Give the extent of all Plasmodium falciparum-infected red blood cells.
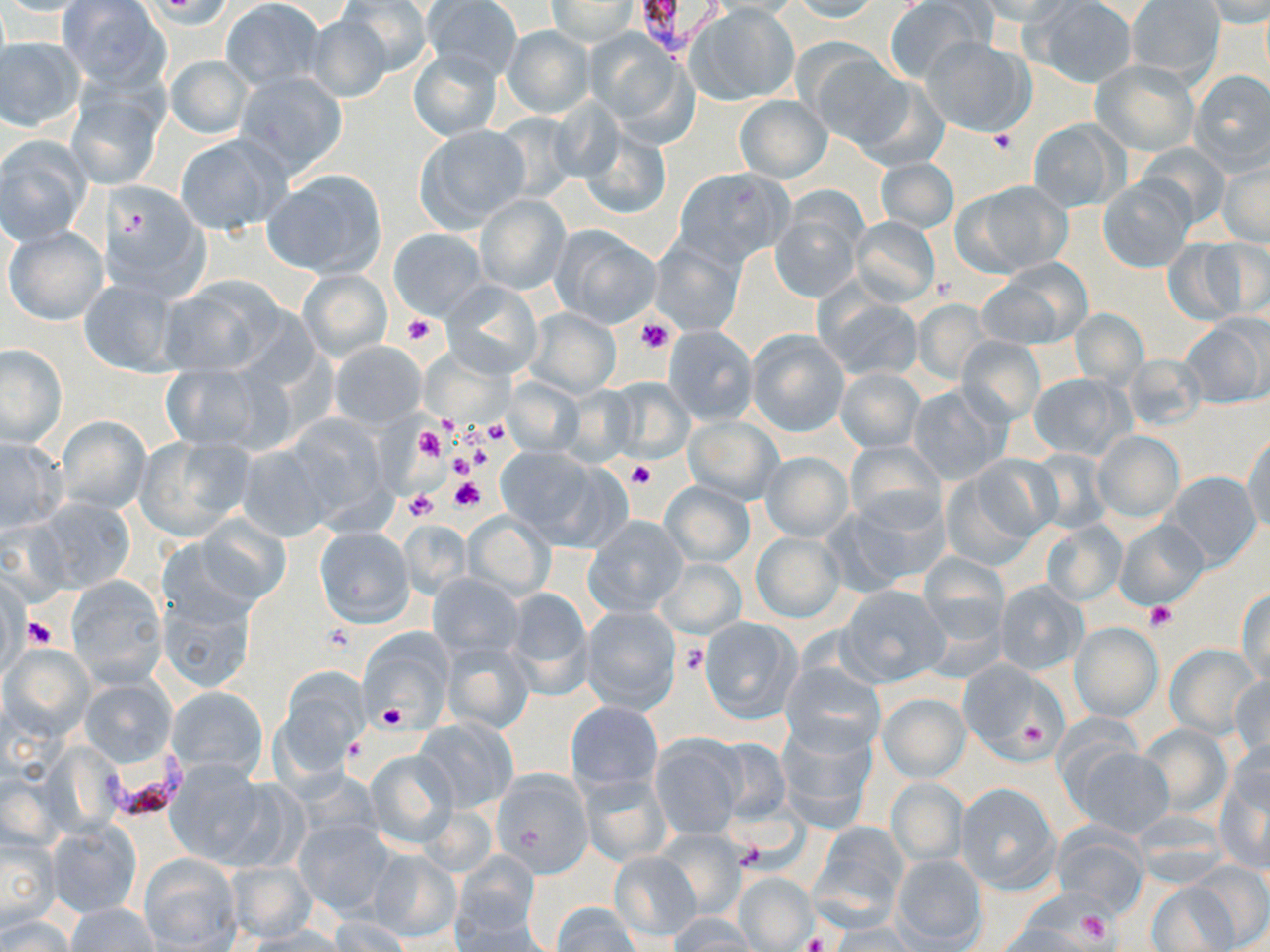
Approximate bounding boxes as named x1/y1/x2/y2 corners in pixels.
Plasmodium falciparum-infected red blood cells: (x1=635, y1=0, x2=724, y2=55), (x1=94, y1=754, x2=197, y2=818).

Summary:
  - Platelet locations: (x1=985, y1=128, x2=1019, y2=156), (x1=402, y1=313, x2=435, y2=346), (x1=637, y1=318, x2=674, y2=355), (x1=483, y1=419, x2=513, y2=445), (x1=414, y1=424, x2=447, y2=463), (x1=446, y1=450, x2=477, y2=478), (x1=627, y1=459, x2=655, y2=488), (x1=448, y1=476, x2=483, y2=512), (x1=406, y1=489, x2=438, y2=520), (x1=1145, y1=601, x2=1177, y2=631), (x1=26, y1=616, x2=55, y2=647), (x1=322, y1=624, x2=354, y2=652), (x1=678, y1=642, x2=709, y2=675), (x1=379, y1=705, x2=406, y2=731), (x1=1015, y1=719, x2=1049, y2=753), (x1=1075, y1=910, x2=1110, y2=944), (x1=803, y1=932, x2=827, y2=952)
  - Uninfected red blood cell locations: (x1=336, y1=0, x2=434, y2=78), (x1=419, y1=0, x2=522, y2=81), (x1=703, y1=0, x2=810, y2=16), (x1=790, y1=0, x2=883, y2=22), (x1=979, y1=0, x2=1076, y2=24), (x1=1125, y1=0, x2=1225, y2=81), (x1=0, y1=1, x2=99, y2=17), (x1=57, y1=1, x2=167, y2=87), (x1=221, y1=1, x2=325, y2=89), (x1=547, y1=1, x2=638, y2=45), (x1=884, y1=1, x2=991, y2=83), (x1=1027, y1=1, x2=1137, y2=88), (x1=1204, y1=1, x2=1270, y2=27), (x1=686, y1=4, x2=799, y2=106), (x1=304, y1=14, x2=393, y2=104), (x1=500, y1=26, x2=593, y2=116), (x1=586, y1=30, x2=692, y2=137), (x1=920, y1=35, x2=1034, y2=137), (x1=0, y1=37, x2=85, y2=132), (x1=804, y1=47, x2=910, y2=148), (x1=407, y1=48, x2=502, y2=141), (x1=164, y1=54, x2=252, y2=138), (x1=1091, y1=60, x2=1198, y2=156), (x1=233, y1=70, x2=349, y2=178), (x1=1189, y1=70, x2=1270, y2=173), (x1=851, y1=75, x2=950, y2=171), (x1=68, y1=82, x2=167, y2=189), (x1=734, y1=95, x2=831, y2=182), (x1=488, y1=111, x2=581, y2=203), (x1=1028, y1=118, x2=1128, y2=212), (x1=414, y1=125, x2=530, y2=232), (x1=580, y1=126, x2=672, y2=221), (x1=173, y1=134, x2=291, y2=236), (x1=0, y1=136, x2=92, y2=244), (x1=1136, y1=145, x2=1231, y2=231), (x1=1218, y1=156, x2=1269, y2=248), (x1=875, y1=157, x2=958, y2=234), (x1=674, y1=166, x2=795, y2=267), (x1=263, y1=168, x2=388, y2=280), (x1=1098, y1=176, x2=1194, y2=273), (x1=955, y1=179, x2=1072, y2=277), (x1=98, y1=181, x2=209, y2=301), (x1=474, y1=194, x2=570, y2=295), (x1=770, y1=197, x2=866, y2=305), (x1=850, y1=216, x2=940, y2=306), (x1=551, y1=225, x2=661, y2=329), (x1=3, y1=226, x2=107, y2=326), (x1=389, y1=228, x2=486, y2=319), (x1=649, y1=235, x2=747, y2=337), (x1=1165, y1=239, x2=1255, y2=325), (x1=979, y1=262, x2=1089, y2=349), (x1=297, y1=269, x2=392, y2=362), (x1=157, y1=275, x2=292, y2=378), (x1=79, y1=276, x2=181, y2=378), (x1=440, y1=279, x2=543, y2=377), (x1=815, y1=289, x2=923, y2=381), (x1=910, y1=299, x2=995, y2=386), (x1=526, y1=308, x2=621, y2=396), (x1=1070, y1=308, x2=1149, y2=387), (x1=1181, y1=316, x2=1268, y2=408), (x1=663, y1=325, x2=758, y2=425), (x1=746, y1=329, x2=850, y2=437), (x1=955, y1=337, x2=1044, y2=426), (x1=330, y1=341, x2=427, y2=430), (x1=1, y1=342, x2=66, y2=447), (x1=1122, y1=354, x2=1206, y2=431), (x1=159, y1=361, x2=286, y2=455), (x1=836, y1=368, x2=924, y2=452), (x1=1027, y1=372, x2=1134, y2=461), (x1=502, y1=376, x2=584, y2=457), (x1=606, y1=377, x2=693, y2=462), (x1=907, y1=384, x2=1008, y2=484), (x1=555, y1=385, x2=639, y2=465), (x1=275, y1=412, x2=397, y2=530), (x1=55, y1=416, x2=151, y2=516), (x1=683, y1=416, x2=783, y2=505), (x1=1091, y1=430, x2=1184, y2=524), (x1=1244, y1=432, x2=1270, y2=535), (x1=134, y1=435, x2=255, y2=540), (x1=0, y1=437, x2=66, y2=532), (x1=844, y1=440, x2=946, y2=531), (x1=235, y1=441, x2=340, y2=542), (x1=493, y1=447, x2=613, y2=547), (x1=1027, y1=449, x2=1114, y2=535), (x1=762, y1=451, x2=853, y2=541), (x1=950, y1=455, x2=1058, y2=557), (x1=1163, y1=471, x2=1261, y2=573), (x1=661, y1=482, x2=754, y2=566), (x1=839, y1=490, x2=951, y2=589), (x1=34, y1=499, x2=135, y2=593), (x1=463, y1=512, x2=554, y2=599), (x1=194, y1=514, x2=290, y2=605), (x1=585, y1=516, x2=687, y2=616), (x1=1115, y1=518, x2=1209, y2=611), (x1=399, y1=520, x2=473, y2=598), (x1=1040, y1=520, x2=1127, y2=606), (x1=314, y1=526, x2=415, y2=628), (x1=750, y1=532, x2=844, y2=622), (x1=917, y1=553, x2=1010, y2=648), (x1=654, y1=559, x2=745, y2=638), (x1=428, y1=573, x2=522, y2=659), (x1=66, y1=577, x2=168, y2=688), (x1=993, y1=580, x2=1087, y2=675), (x1=837, y1=584, x2=950, y2=687), (x1=504, y1=587, x2=593, y2=697), (x1=157, y1=588, x2=259, y2=696), (x1=1237, y1=588, x2=1269, y2=684), (x1=581, y1=606, x2=679, y2=713), (x1=700, y1=617, x2=802, y2=724), (x1=1070, y1=622, x2=1163, y2=721), (x1=359, y1=626, x2=453, y2=725), (x1=443, y1=643, x2=534, y2=735), (x1=1165, y1=643, x2=1262, y2=739), (x1=4, y1=644, x2=94, y2=741), (x1=957, y1=659, x2=1065, y2=762), (x1=779, y1=661, x2=886, y2=758), (x1=277, y1=668, x2=368, y2=770), (x1=1228, y1=675, x2=1269, y2=765), (x1=79, y1=677, x2=178, y2=768), (x1=167, y1=686, x2=267, y2=779), (x1=878, y1=692, x2=971, y2=782), (x1=566, y1=701, x2=663, y2=794), (x1=415, y1=718, x2=517, y2=812), (x1=776, y1=723, x2=878, y2=833), (x1=1137, y1=723, x2=1232, y2=818), (x1=649, y1=736, x2=745, y2=839), (x1=711, y1=738, x2=791, y2=823), (x1=1227, y1=738, x2=1269, y2=819), (x1=1072, y1=747, x2=1173, y2=838), (x1=365, y1=749, x2=458, y2=848), (x1=1216, y1=754, x2=1270, y2=871), (x1=170, y1=765, x2=289, y2=869), (x1=495, y1=771, x2=592, y2=875), (x1=579, y1=772, x2=673, y2=868), (x1=885, y1=780, x2=968, y2=866), (x1=953, y1=783, x2=1058, y2=892), (x1=295, y1=817, x2=395, y2=916), (x1=46, y1=820, x2=143, y2=917), (x1=809, y1=824, x2=910, y2=931), (x1=1050, y1=824, x2=1149, y2=915), (x1=1, y1=828, x2=60, y2=930), (x1=655, y1=831, x2=745, y2=919), (x1=367, y1=849, x2=462, y2=942), (x1=453, y1=851, x2=540, y2=940), (x1=609, y1=852, x2=701, y2=941), (x1=138, y1=853, x2=241, y2=950), (x1=893, y1=854, x2=987, y2=949), (x1=229, y1=860, x2=315, y2=943), (x1=1186, y1=861, x2=1270, y2=950), (x1=733, y1=872, x2=815, y2=950), (x1=1146, y1=879, x2=1240, y2=952), (x1=450, y1=902, x2=550, y2=951), (x1=551, y1=902, x2=642, y2=952), (x1=65, y1=903, x2=160, y2=952), (x1=327, y1=915, x2=413, y2=951), (x1=0, y1=916, x2=74, y2=951), (x1=668, y1=916, x2=757, y2=951), (x1=996, y1=920, x2=1093, y2=951), (x1=239, y1=925, x2=354, y2=952), (x1=826, y1=925, x2=927, y2=951)
  - Slide-level diagnosis: Plasmodium falciparum
  - Magnification: 1000x
  - Preparation: thin blood smear
  - Modality: light microscopy
  - Stain: May-Grünwald-Giemsa
  - Image size: 1270×952 pixels
  - Field of view: single